Classify this cell by malaria status.
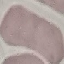

Uninfected.

Thin smear of blood. Photographed with a smartphone camera at the microscope eyepiece. Giemsa stain. Cell patch, automatically extracted from a larger field of view and resized to 64 × 64 pixels.